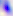

Summary:
  - Magnification: 400x
  - Identification: Toxoplasma gondii
  - Modality: micrograph